Assess this cell for malaria.
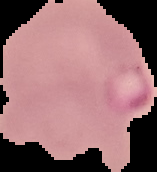

It is parasitized.

preparation: thin blood smear
image_type: segmented cell region on a black background
image_size: 157×172 pixels